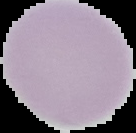
Summary:
  - Preparation: thin blood film
  - Result: negative for malaria parasites
  - Image size: 136×133 pixels
  - Image type: segmented cell region with the area outside set to black